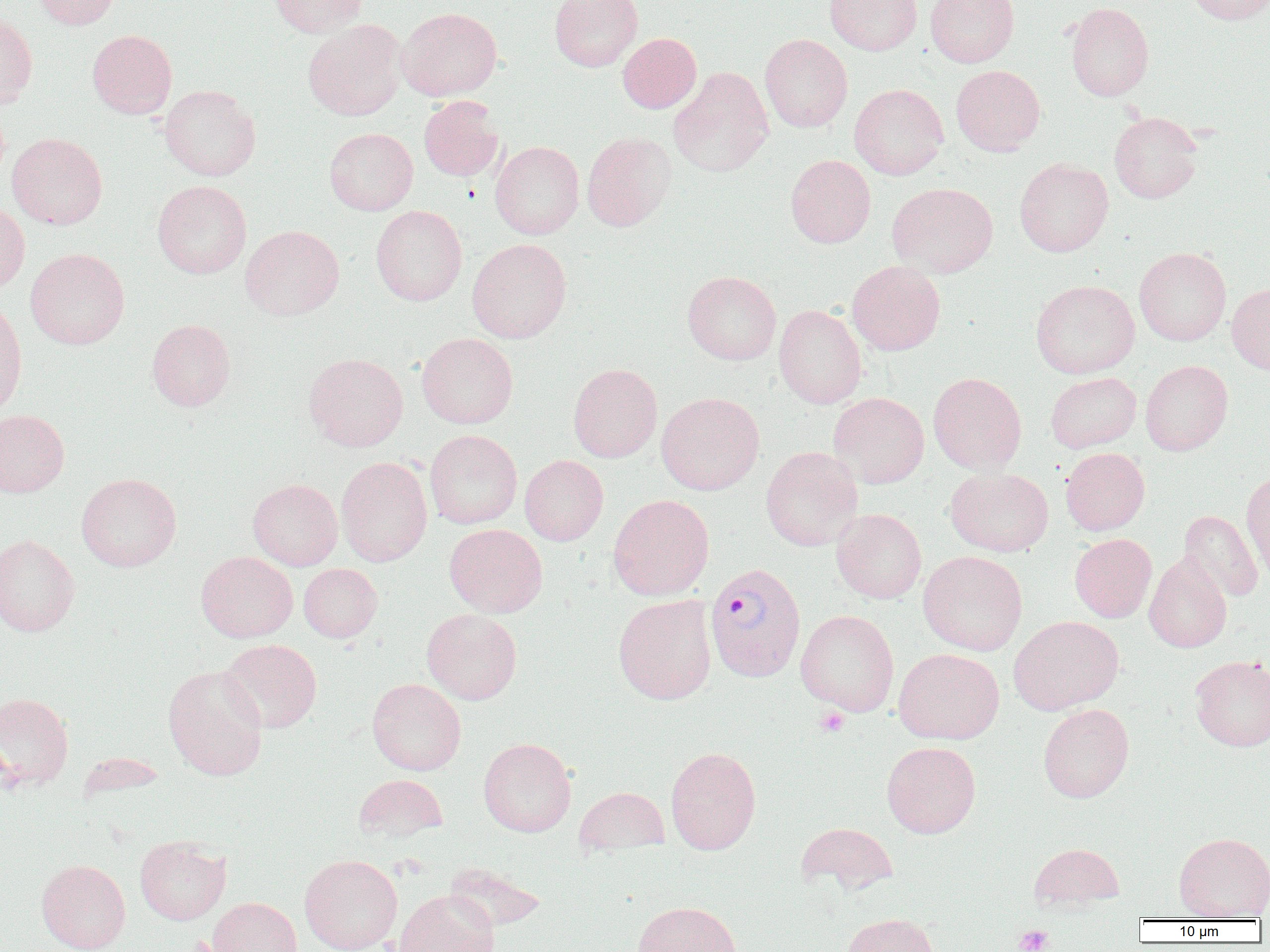

Approximate bounding boxes as (x1, y1, x2, y2) in pixels. Plasmodium vivax-infected red blood cell locations: (704, 562, 806, 683). Uninfected red blood cell locations: (32, 0, 121, 29), (267, 0, 368, 37), (549, 0, 643, 72), (824, 0, 922, 55), (926, 0, 1019, 67), (1184, 0, 1270, 25), (1066, 2, 1154, 102), (397, 7, 502, 100), (0, 12, 37, 110), (303, 19, 407, 121), (87, 29, 177, 118), (617, 33, 702, 113), (759, 34, 853, 132), (951, 65, 1045, 156), (669, 67, 773, 178), (849, 84, 948, 180), (160, 85, 261, 181), (418, 96, 504, 181), (1109, 112, 1203, 204), (324, 127, 418, 215), (582, 131, 676, 231), (7, 133, 107, 230), (490, 141, 584, 239), (785, 155, 876, 248), (1014, 158, 1114, 256), (152, 180, 252, 279), (887, 183, 998, 278), (0, 202, 30, 294), (371, 205, 467, 306), (240, 225, 344, 320), (467, 238, 572, 343), (1134, 246, 1231, 346), (25, 248, 129, 349), (847, 261, 945, 355), (682, 271, 781, 365), (1030, 280, 1140, 379), (1226, 283, 1270, 375), (0, 300, 27, 418), (774, 305, 866, 409), (146, 318, 236, 411), (417, 333, 518, 429), (303, 353, 408, 451), (1140, 360, 1233, 456), (568, 363, 662, 462), (928, 372, 1027, 474), (1045, 372, 1141, 453), (656, 392, 765, 495), (829, 392, 929, 489), (0, 410, 69, 497), (425, 429, 522, 529), (761, 446, 863, 551), (1060, 447, 1150, 535), (520, 455, 608, 546), (336, 456, 433, 566), (945, 467, 1053, 557), (1240, 471, 1270, 583), (76, 473, 181, 572), (247, 479, 343, 570), (608, 494, 714, 601), (831, 508, 926, 604), (1178, 510, 1264, 602), (444, 523, 547, 617), (1070, 533, 1157, 622), (0, 534, 80, 637), (918, 550, 1028, 656), (196, 551, 298, 642), (1144, 552, 1232, 653), (298, 563, 382, 642), (614, 594, 717, 705), (422, 609, 522, 704), (796, 610, 899, 716), (1008, 615, 1124, 715), (219, 639, 322, 733), (893, 648, 1004, 744), (1189, 655, 1270, 752), (162, 664, 268, 781), (367, 678, 466, 775), (0, 692, 74, 790), (1038, 703, 1134, 802), (478, 737, 576, 837), (882, 741, 981, 838), (665, 746, 761, 854), (353, 774, 448, 843), (574, 787, 669, 856), (796, 821, 899, 894), (1174, 832, 1270, 920), (135, 836, 231, 925), (1028, 842, 1125, 912), (299, 854, 403, 952), (36, 859, 131, 952), (442, 862, 547, 932), (393, 889, 499, 952), (208, 897, 301, 952), (632, 900, 742, 952), (843, 912, 941, 952). Platelet locations: (815, 706, 850, 737), (1013, 924, 1055, 952). Slide-level diagnosis: Plasmodium vivax. Thin blood smear. Single field of view. Image is 1270×952 pixels. Captured at 1000x magnification. Light microscopy.